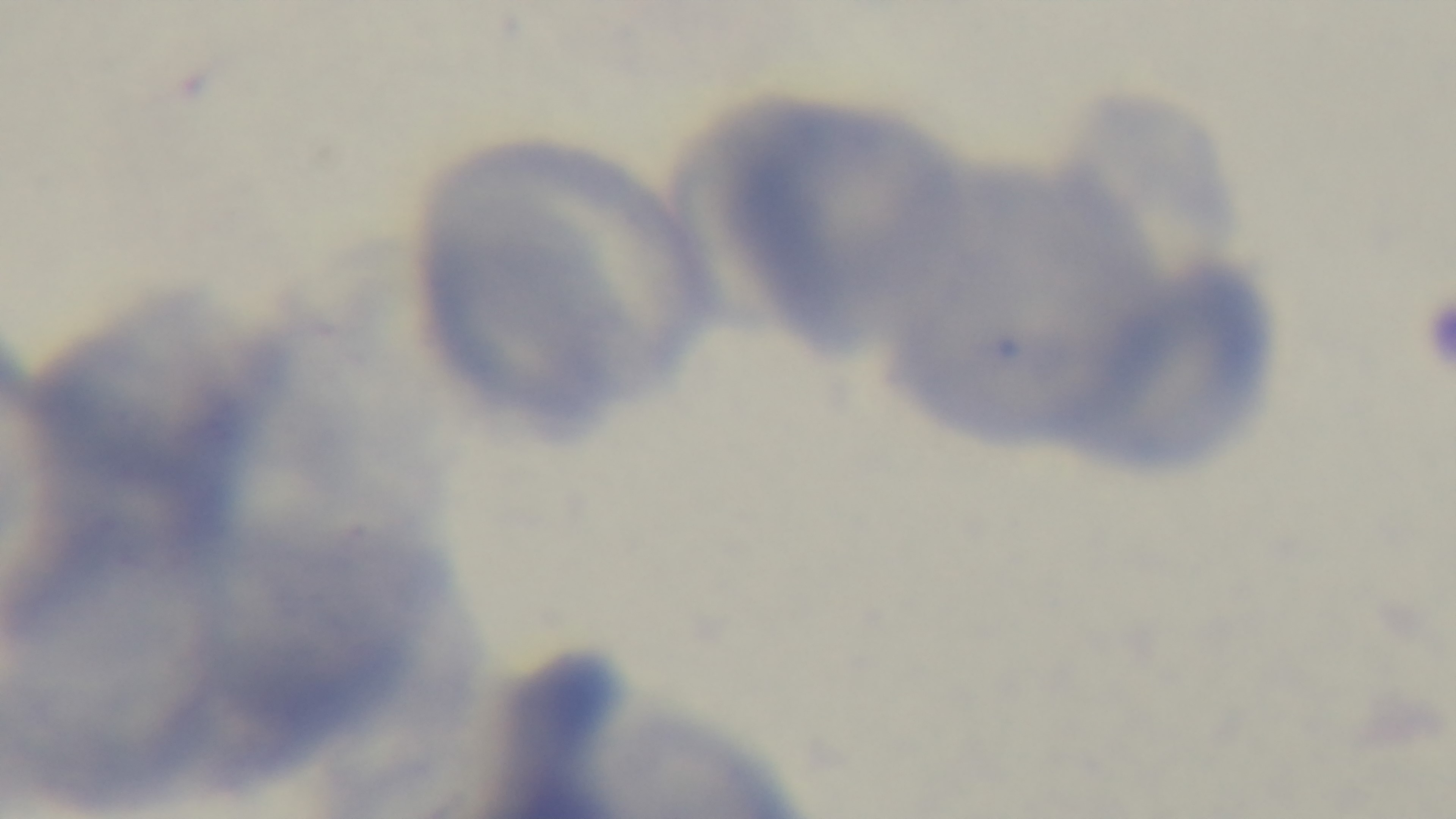 Light microscopy. Malaria status: uninfected. 100x oil-immersion objective. Giemsa-stained. Preparation: thin. Captured with a mounted 4K digital camera. Single field of view.